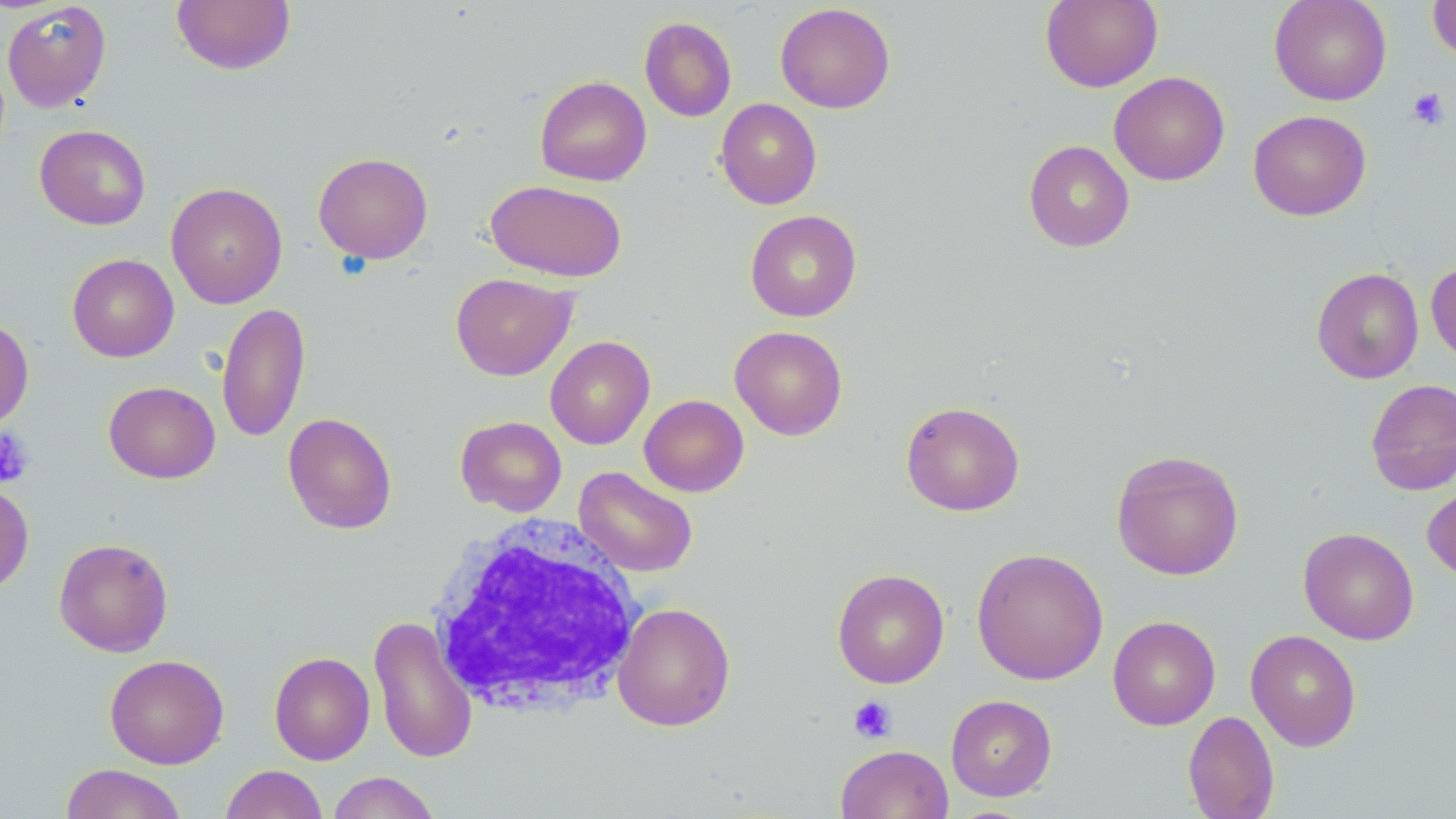

slide-level diagnosis = negative for blood parasites
stain = May-Grünwald-Giemsa
modality = light microscopy
white blood cell locations = approximate bounding boxes as named x1/y1/x2/y2 corners in pixels: (x1=426, y1=515, x2=645, y2=719)
image size = 1456×819 pixels
preparation = thin blood smear
field of view = one of a larger specimen
platelet locations = approximate bounding boxes as named x1/y1/x2/y2 corners in pixels: (x1=1407, y1=87, x2=1450, y2=130), (x1=0, y1=427, x2=35, y2=487), (x1=848, y1=696, x2=897, y2=743)
uninfected red blood cell locations = approximate bounding boxes as named x1/y1/x2/y2 corners in pixels: (x1=1040, y1=0, x2=1162, y2=92), (x1=1269, y1=0, x2=1392, y2=105), (x1=1427, y1=0, x2=1456, y2=64), (x1=2, y1=1, x2=111, y2=112), (x1=172, y1=1, x2=295, y2=75), (x1=775, y1=3, x2=896, y2=114), (x1=640, y1=16, x2=737, y2=122), (x1=1109, y1=71, x2=1230, y2=186), (x1=534, y1=75, x2=652, y2=187), (x1=715, y1=98, x2=822, y2=209), (x1=1248, y1=110, x2=1371, y2=221), (x1=34, y1=124, x2=151, y2=230), (x1=1023, y1=140, x2=1135, y2=252), (x1=313, y1=152, x2=433, y2=264), (x1=486, y1=179, x2=628, y2=282), (x1=166, y1=182, x2=288, y2=309), (x1=745, y1=209, x2=862, y2=322), (x1=67, y1=254, x2=178, y2=362), (x1=1426, y1=260, x2=1456, y2=366), (x1=1311, y1=267, x2=1424, y2=384), (x1=450, y1=273, x2=576, y2=380), (x1=217, y1=301, x2=311, y2=444), (x1=0, y1=317, x2=34, y2=431), (x1=729, y1=325, x2=848, y2=440), (x1=545, y1=335, x2=655, y2=449), (x1=1365, y1=378, x2=1456, y2=495), (x1=103, y1=381, x2=220, y2=483), (x1=639, y1=394, x2=749, y2=497), (x1=901, y1=400, x2=1025, y2=516), (x1=283, y1=412, x2=397, y2=534), (x1=455, y1=415, x2=567, y2=517), (x1=1111, y1=449, x2=1244, y2=581), (x1=573, y1=466, x2=698, y2=578), (x1=0, y1=481, x2=34, y2=597), (x1=1423, y1=483, x2=1456, y2=582), (x1=1298, y1=527, x2=1419, y2=645), (x1=53, y1=537, x2=174, y2=656), (x1=971, y1=547, x2=1109, y2=685), (x1=832, y1=568, x2=950, y2=688), (x1=613, y1=602, x2=735, y2=731), (x1=368, y1=615, x2=479, y2=764), (x1=1107, y1=615, x2=1221, y2=731), (x1=1245, y1=629, x2=1361, y2=751), (x1=269, y1=651, x2=375, y2=765), (x1=104, y1=654, x2=229, y2=769), (x1=945, y1=694, x2=1057, y2=801), (x1=1182, y1=710, x2=1279, y2=819), (x1=835, y1=744, x2=954, y2=819), (x1=60, y1=763, x2=188, y2=819), (x1=221, y1=764, x2=328, y2=819), (x1=326, y1=771, x2=441, y2=819)
magnification = 1000x